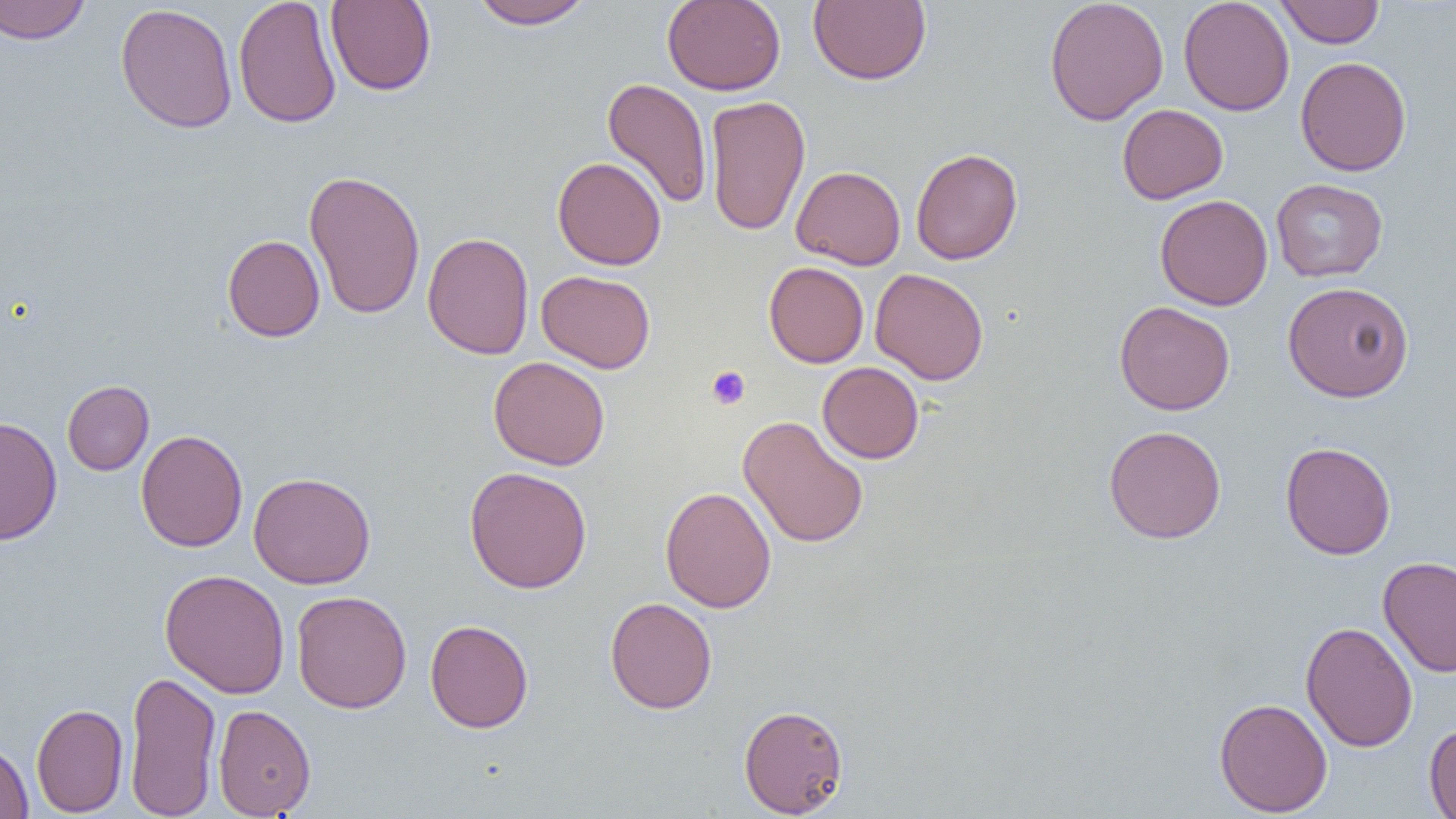 Approximate bounding boxes as (x1,y1)-(x2,y2) corner pairs in pixels. Uninfected red blood cell locations: (0,0)-(91,44), (233,0)-(342,129), (325,0)-(436,96), (468,0)-(594,30), (662,0)-(786,95), (809,0)-(932,85), (1044,0)-(1169,126), (1178,0)-(1294,116), (1276,1)-(1385,48), (115,3)-(238,134), (1296,56)-(1412,177), (602,77)-(713,209), (705,95)-(811,237), (1117,104)-(1228,204), (910,148)-(1022,265), (552,156)-(666,270), (791,165)-(906,270), (304,169)-(426,320), (1270,178)-(1388,282), (1155,194)-(1273,311), (422,231)-(534,360), (222,234)-(325,342), (764,261)-(868,368), (870,267)-(989,385), (536,270)-(656,373), (1282,281)-(1414,402), (1114,301)-(1235,415), (488,356)-(610,470), (817,362)-(924,464), (62,380)-(154,475), (738,415)-(869,548), (1,416)-(63,545), (1103,425)-(1226,544), (135,429)-(248,552), (1280,441)-(1396,559), (464,466)-(592,594), (248,471)-(376,589), (660,486)-(776,614), (1378,555)-(1456,678), (159,569)-(290,699), (291,590)-(411,714), (604,596)-(717,714), (425,619)-(534,733), (1300,621)-(1418,752), (125,669)-(221,819), (1214,697)-(1333,816), (31,702)-(128,816), (739,703)-(849,817), (213,704)-(316,817), (1424,722)-(1456,818), (0,740)-(33,818). Platelet locations: (706,366)-(751,410). Slide-level diagnosis: negative for blood parasites. Thin blood smear. 1000x magnification. One field of a larger specimen. Image is 1456×819 pixels. Optical microscopy.